Locate every blood parasite and identify its species.
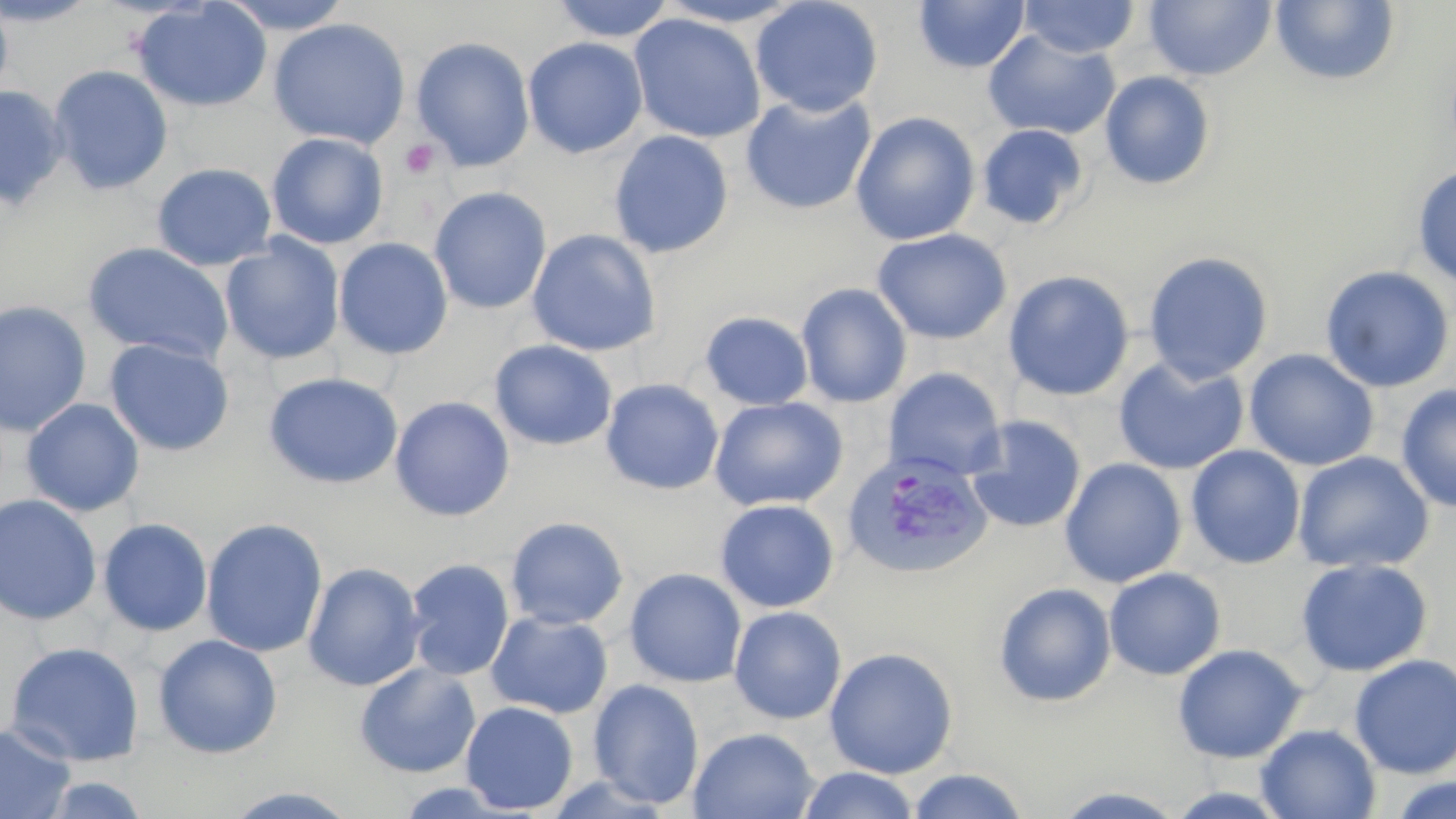

Approximate bounding boxes as (x1,y1)-(x2,y2) corner pairs in pixels.
Plasmodium vivax-infected red blood cells: (841,450)-(993,580).
No Plasmodium falciparum, Plasmodium ovale, Plasmodium malariae, Babesia divergens, or Trypanosoma brucei observed.

slide_level_diagnosis: Plasmodium vivax
modality: optical microscopy
magnification: 1000x
image_size: 1456×819 pixels
field_of_view: single
platelet_locations: 'approximate bounding boxes as (x1,y1)-(x2,y2) corner pairs in pixels: (399,139)-(438,179)'
uninfected_red_blood_cell_locations: 'approximate bounding boxes as (x1,y1)-(x2,y2) corner pairs in pixels: (0,0)-(14,106), (0,0)-(101,26), (131,0)-(273,113), (218,0)-(356,33), (551,0)-(676,42), (750,0)-(884,117), (913,0)-(1030,73), (1018,1)-(1141,59), (1143,1)-(1276,81), (1270,1)-(1400,86), (628,13)-(766,143), (268,18)-(411,149), (982,30)-(1121,140), (410,37)-(535,172), (522,37)-(648,158), (48,64)-(174,195), (1099,70)-(1216,189), (0,84)-(69,209), (740,92)-(876,215), (850,112)-(980,245), (977,124)-(1089,230), (609,130)-(733,258), (267,132)-(389,249), (151,162)-(277,270), (1412,165)-(1456,289), (429,187)-(551,314), (872,228)-(1012,344), (527,229)-(661,356), (220,234)-(345,365), (334,237)-(453,359), (82,242)-(234,364), (1142,250)-(1274,384), (1319,265)-(1455,392), (1003,270)-(1135,401), (795,283)-(912,408), (0,299)-(93,436), (700,312)-(814,410), (103,338)-(234,456), (489,340)-(618,451), (1244,349)-(1380,472), (1113,356)-(1249,475), (884,367)-(1006,482), (263,371)-(404,489), (600,378)-(724,495), (1396,384)-(1456,512), (389,396)-(515,521), (708,397)-(848,512), (21,398)-(145,517), (964,415)-(1086,534), (1186,445)-(1306,569), (1292,451)-(1434,574), (1060,457)-(1187,587), (0,494)-(102,625), (714,499)-(840,613), (505,516)-(629,630), (97,517)-(213,637), (201,518)-(328,657), (1295,557)-(1433,677), (404,558)-(515,680), (303,562)-(426,692), (1104,567)-(1226,681), (624,568)-(747,687), (993,582)-(1116,707), (728,606)-(847,725), (486,611)-(613,719), (152,633)-(283,759), (4,641)-(145,767), (1172,644)-(1307,763), (823,646)-(959,779), (1349,654)-(1456,778), (354,662)-(482,778), (588,678)-(704,809), (460,700)-(578,814), (0,721)-(76,819), (1256,723)-(1381,818), (688,726)-(819,819), (797,767)-(921,819), (906,768)-(1031,819), (37,773)-(155,818), (1386,774)-(1455,819), (1045,784)-(1192,818), (221,786)-(363,818)'
stain: May-Grünwald-Giemsa
preparation: thin blood smear